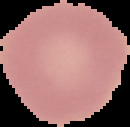

image size = 130×127 pixels
preparation = thin blood smear
image type = segmented cell region on a black background
result = negative for malaria parasites